Give the position of every leukocyte visible.
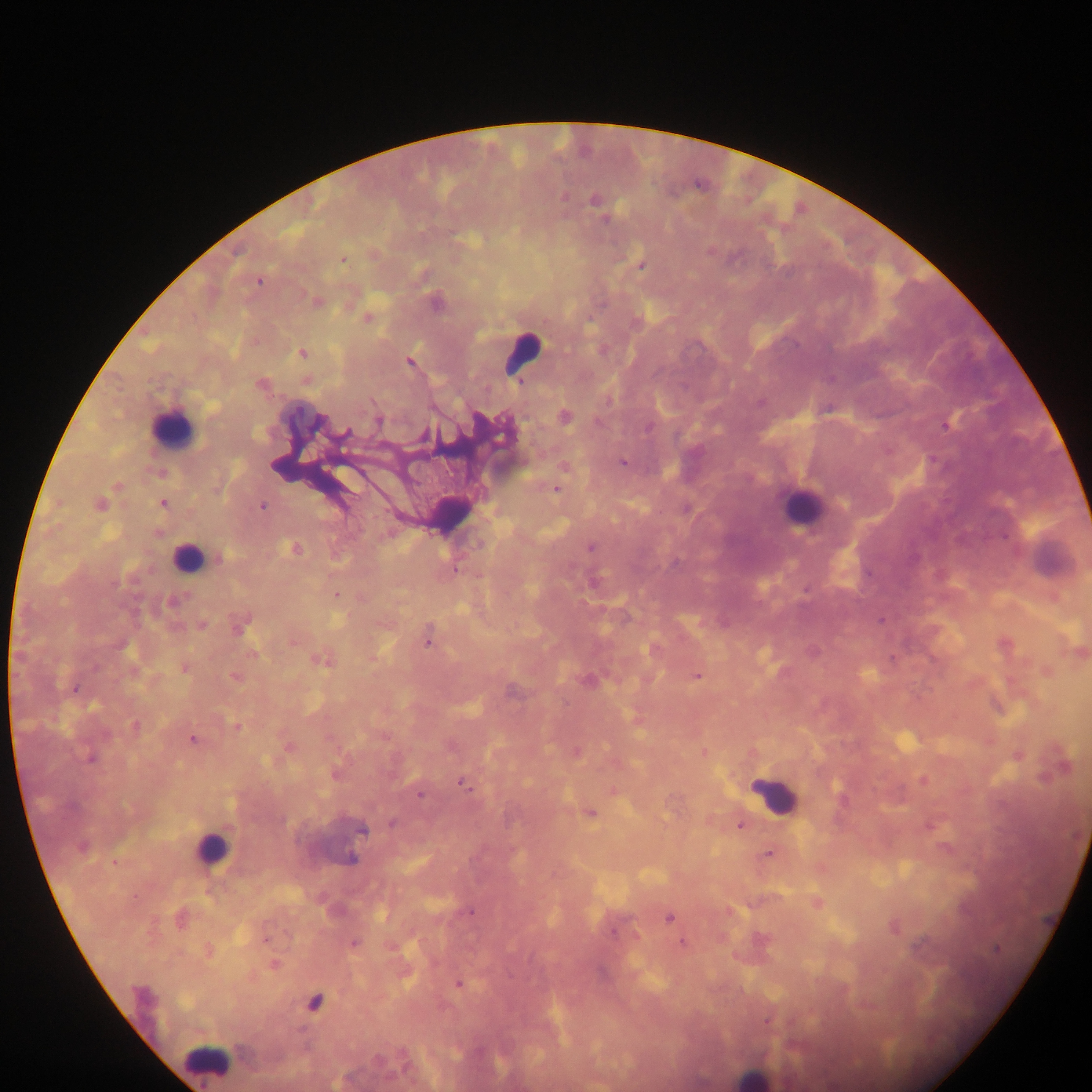

Approximate centers as {x, y} in pixels.
Leukocytes: {521, 354}, {173, 428}, {802, 508}, {451, 513}, {187, 558}, {774, 796}, {212, 850}, {207, 1061}, {753, 1077}.

malaria_parasite_locations: 'approximate centers as {x, y} in pixels: {563, 196}, {596, 201}, {604, 219}, {710, 251}, {343, 259}, {642, 265}, {259, 281}, {316, 302}, {435, 303}, {367, 318}, {302, 353}, {409, 361}, {307, 380}, {261, 384}, {564, 417}, {378, 420}, {946, 424}, {345, 433}, {623, 462}, {564, 467}, {555, 488}, {162, 503}, {99, 504}, {262, 506}, {590, 547}, {294, 548}, {217, 558}, {335, 595}, {172, 601}, {881, 619}, {240, 624}, {201, 625}, {429, 636}, {293, 640}, {1004, 644}, {653, 650}, {1079, 651}, {322, 658}, {184, 668}, {1046, 671}, {697, 675}, {233, 677}, {75, 688}, {512, 691}, {995, 705}, {135, 726}, {236, 727}, {193, 739}, {287, 747}, {576, 752}, {703, 752}, {1017, 755}, {91, 758}, {1061, 766}, {336, 773}, {923, 780}, {464, 784}, {612, 790}, {420, 794}, {590, 813}, {393, 823}, {740, 824}, {930, 825}, {361, 829}, {81, 846}, {769, 853}, {350, 859}, {114, 862}, {816, 903}, {470, 912}, {669, 917}, {179, 918}, {894, 927}, {265, 939}, {683, 942}, {354, 943}, {208, 951}, {273, 963}, {457, 984}, {314, 1003}, {768, 1020}'
image_size: 1092×1092 pixels
country: Ghana
preparation: thick blood film
field_of_view: single
capture: mobile-phone photograph through a microscope